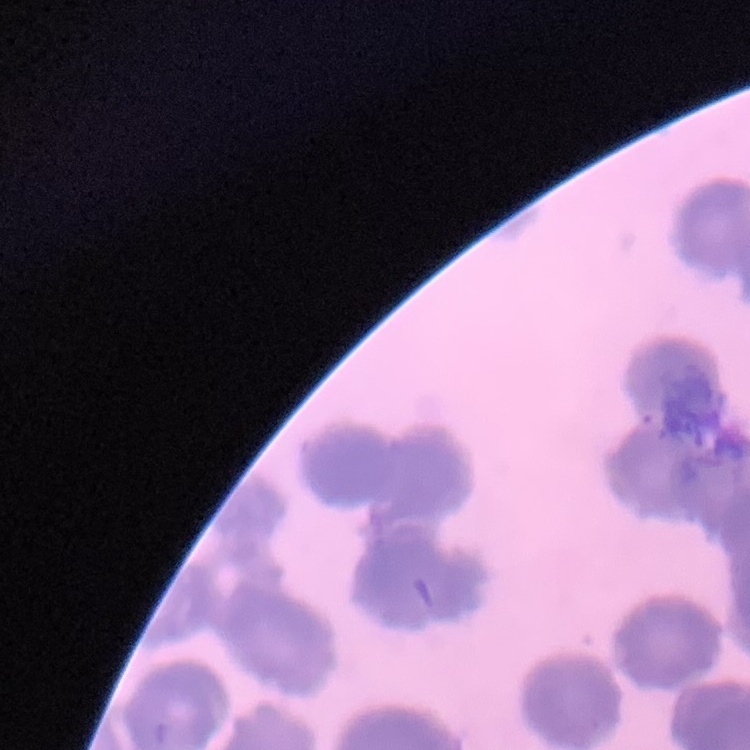
erythrocyte_morphology: rouleaux formation
preparation: thin peripheral smear
image_type: square crop of a larger photomicrograph
stain: Field's or Giemsa